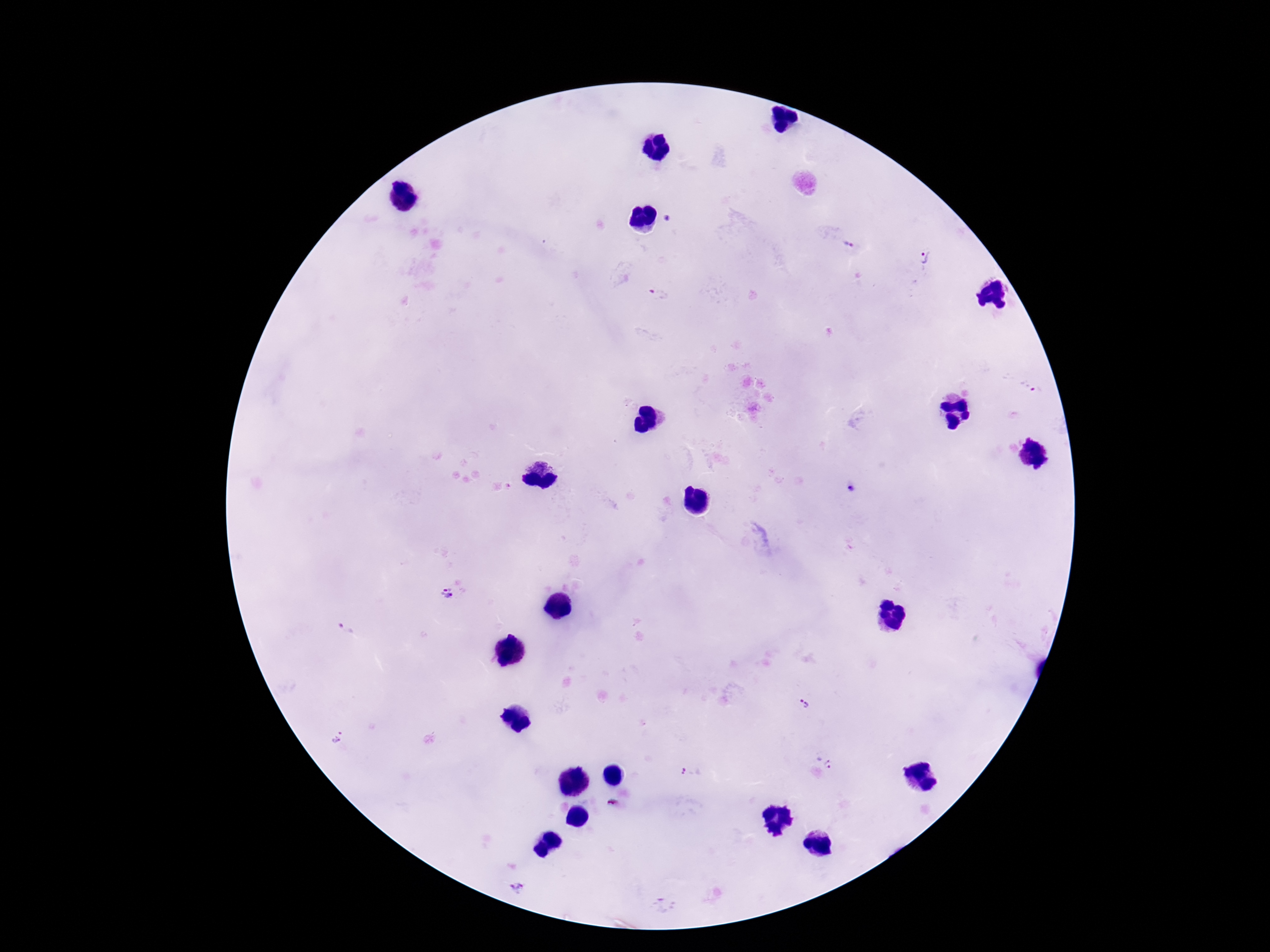

{
  "magnification": "100x",
  "preparation": "thick blood film",
  "patient_malaria_status": "infected",
  "stain": "Giemsa",
  "field_of_view": "one from this slide",
  "image_size": "1270×952 pixels",
  "plasmodium_parasite_locations": "approximate centers as [x, y] in pixels: [850, 243], [927, 258], [659, 293], [1038, 392], [447, 593], [346, 630], [804, 704], [335, 737], [832, 763], [692, 771], [614, 805], [518, 887], [664, 906]",
  "capture": "smartphone camera through the microscope eyepiece"
}